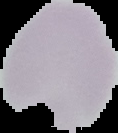
Summary:
  - Preparation: thin blood film
  - Image type: segmented cell region with the area outside set to black
  - Malaria status: uninfected
  - Image size: 118×133 pixels